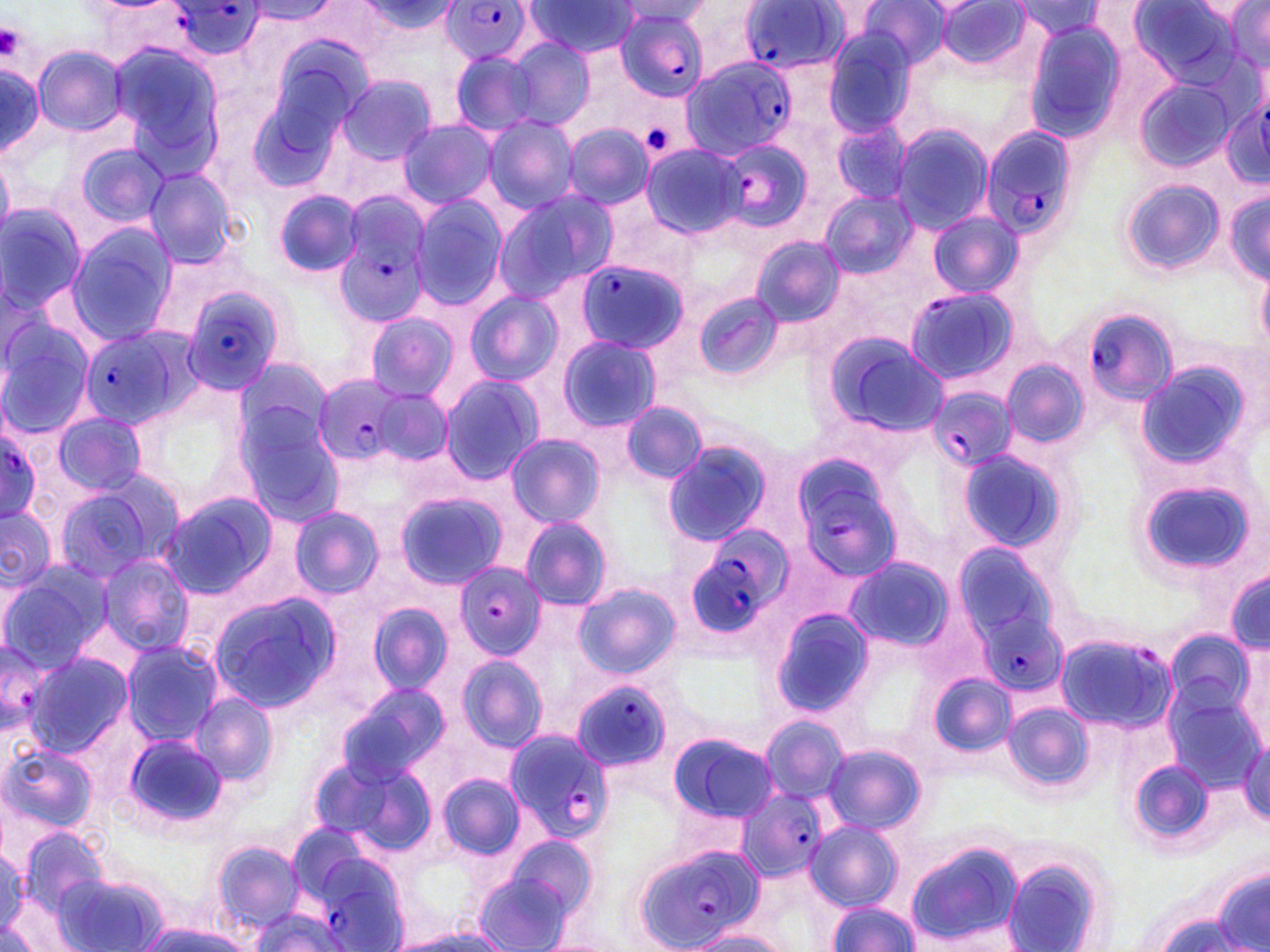
Summary:
  - Coordinate format: approximate bounding boxes as (x1, y1, x2, y2) in pixels
  - Platelet locations: (0, 22, 23, 59), (643, 120, 672, 152)
  - Uninfected red blood cell locations: (247, 0, 337, 26), (354, 0, 459, 40), (1015, 0, 1102, 42), (615, 1, 713, 25), (933, 1, 1034, 71), (523, 2, 641, 57), (853, 2, 951, 71), (1129, 2, 1243, 87), (681, 3, 766, 82), (1223, 3, 1270, 75), (1022, 21, 1129, 141), (821, 29, 922, 136), (503, 35, 597, 131), (107, 41, 223, 174), (33, 47, 126, 135), (249, 49, 371, 186), (449, 49, 543, 137), (0, 61, 45, 157), (337, 74, 437, 166), (1134, 80, 1238, 173), (483, 116, 578, 213), (397, 119, 500, 208), (830, 121, 913, 204), (890, 122, 993, 233), (564, 124, 656, 207), (75, 143, 170, 226), (641, 144, 745, 239), (142, 165, 241, 269), (1120, 179, 1225, 276), (1225, 186, 1269, 285), (273, 189, 364, 278), (492, 189, 616, 300), (820, 191, 916, 278), (411, 195, 507, 309), (0, 203, 87, 315), (926, 212, 1023, 298), (66, 222, 178, 340), (750, 235, 846, 328), (1256, 264, 1270, 351), (465, 290, 563, 386), (694, 292, 785, 381), (365, 313, 458, 401), (0, 319, 93, 436), (818, 331, 947, 436), (558, 336, 660, 432), (233, 355, 333, 458), (1001, 358, 1087, 449), (1137, 361, 1253, 472), (439, 375, 543, 486), (373, 386, 451, 467), (619, 401, 706, 485), (235, 406, 347, 526), (52, 411, 150, 496), (504, 434, 604, 529), (660, 440, 773, 547), (955, 447, 1072, 556), (52, 477, 177, 583), (1137, 479, 1255, 579), (394, 491, 507, 588), (159, 492, 278, 599), (0, 505, 56, 587), (289, 506, 383, 599), (519, 516, 612, 610), (951, 541, 1064, 646), (97, 556, 193, 656), (844, 557, 953, 654), (0, 565, 109, 672), (1227, 568, 1269, 655), (574, 583, 680, 679), (208, 592, 342, 713), (367, 602, 452, 695), (769, 606, 875, 719), (1165, 629, 1258, 722), (120, 639, 224, 745), (25, 652, 133, 757), (456, 656, 546, 755), (930, 674, 1015, 756), (340, 683, 449, 783), (189, 693, 277, 787), (1003, 702, 1094, 791), (758, 714, 850, 804), (121, 731, 229, 832), (666, 731, 777, 824), (1240, 737, 1270, 823), (823, 742, 924, 835), (1, 744, 97, 834), (308, 753, 432, 854), (1128, 759, 1216, 845), (438, 773, 524, 860), (805, 820, 904, 910), (13, 826, 111, 923), (495, 835, 599, 927), (211, 840, 306, 931), (905, 841, 1024, 948), (0, 845, 25, 931), (1002, 856, 1109, 952), (1211, 865, 1270, 952), (473, 868, 578, 952), (55, 872, 164, 949), (825, 902, 922, 951), (245, 909, 348, 952), (1148, 914, 1244, 952), (136, 920, 254, 951), (392, 928, 514, 951), (686, 931, 792, 952), (534, 936, 623, 952)
  - Plasmodium falciparum-infected red blood cell locations: (439, 0, 536, 66), (167, 2, 266, 59), (737, 3, 847, 74), (614, 7, 708, 100), (680, 56, 793, 158), (1222, 99, 1270, 191), (978, 122, 1079, 242), (717, 138, 814, 233), (333, 200, 431, 328), (572, 259, 687, 354), (901, 285, 1019, 386), (182, 286, 291, 398), (1085, 308, 1178, 404), (79, 329, 188, 427), (312, 374, 413, 465), (929, 384, 1015, 473), (0, 431, 43, 522), (790, 453, 906, 584), (682, 527, 791, 641), (453, 563, 546, 660), (977, 606, 1071, 695), (1055, 632, 1176, 734), (0, 637, 53, 735), (570, 682, 672, 772), (502, 729, 612, 843), (735, 786, 829, 882), (297, 839, 412, 949), (635, 843, 761, 952)
  - Slide-level diagnosis: Plasmodium falciparum
  - Modality: optical microscopy
  - Magnification: 1000x
  - Stain: May-Grünwald-Giemsa
  - Field of view: single
  - Preparation: thin blood film
  - Image size: 1270×952 pixels